Report the malaria status of this cell.
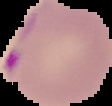
It is parasitized.

Cell region segmented out of the field of view; the surrounding area is masked to black. From a thin blood film. Image is 112×106 pixels.